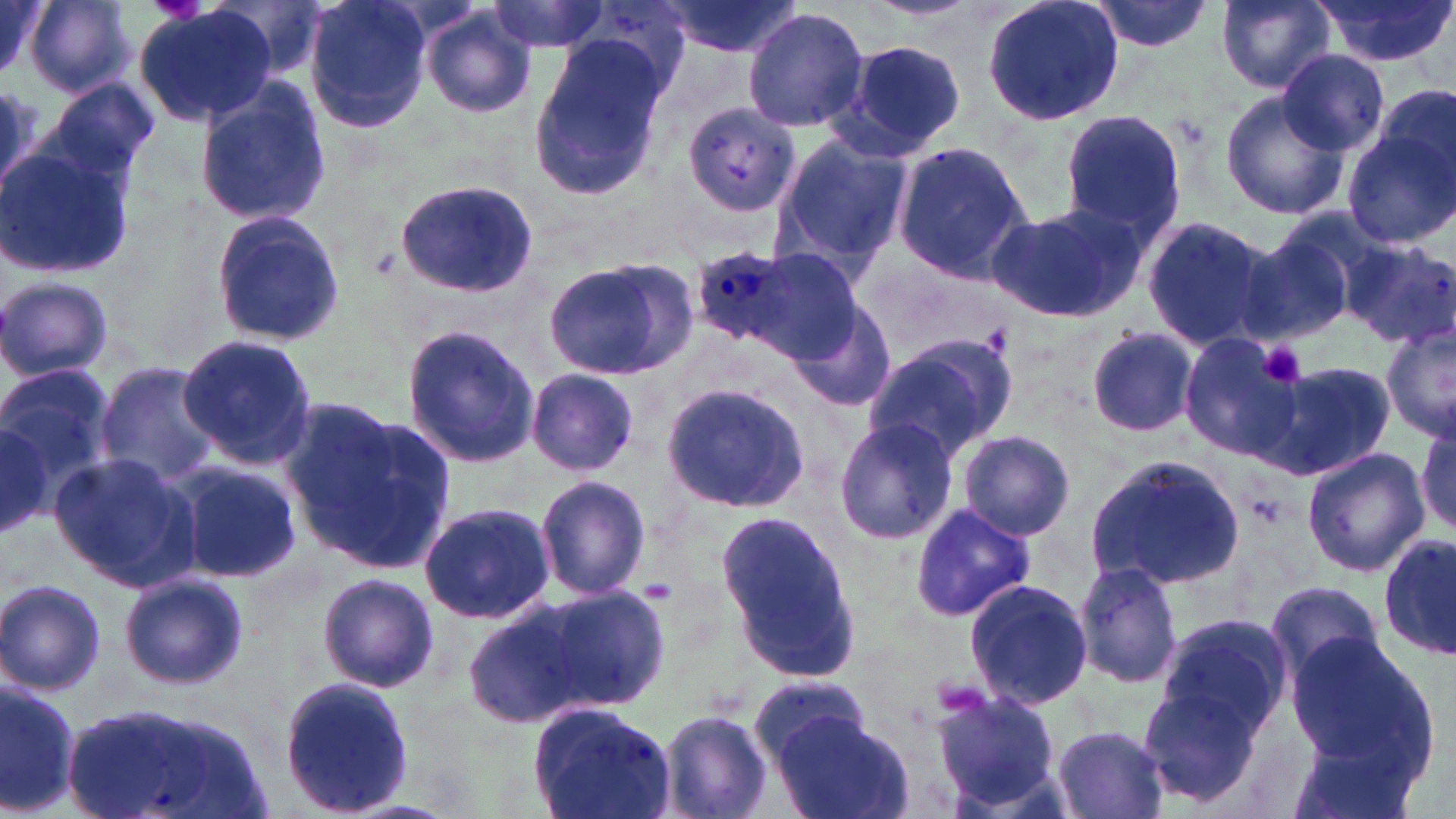 Approximate bounding boxes as [x1, y1, x2, y2] in pixels. Plasmodium ovale-infected red blood cell locations: [693, 245, 795, 345]. Uninfected red blood cell locations: [0, 0, 44, 78], [26, 0, 133, 96], [211, 0, 332, 81], [304, 0, 434, 136], [657, 0, 808, 59], [980, 0, 1124, 126], [1089, 0, 1214, 55], [1214, 0, 1339, 92], [1309, 0, 1455, 68], [484, 1, 615, 55], [135, 6, 276, 128], [420, 8, 537, 119], [743, 8, 870, 135], [527, 36, 671, 200], [835, 39, 966, 163], [1277, 49, 1388, 157], [0, 78, 57, 192], [41, 78, 159, 187], [194, 81, 331, 226], [1367, 82, 1456, 212], [1218, 93, 1349, 220], [679, 103, 804, 221], [1058, 110, 1186, 236], [1340, 124, 1456, 249], [773, 134, 912, 268], [890, 139, 1034, 286], [0, 143, 134, 280], [394, 179, 537, 298], [988, 202, 1145, 323], [210, 210, 344, 346], [1141, 215, 1276, 353], [1232, 231, 1357, 349], [1339, 239, 1455, 347], [766, 251, 857, 367], [544, 256, 699, 382], [0, 276, 115, 380], [790, 303, 899, 412], [399, 323, 543, 472], [1382, 325, 1456, 444], [1083, 326, 1199, 438], [177, 333, 320, 471], [862, 334, 1015, 460], [1178, 335, 1304, 460], [1266, 361, 1395, 481], [0, 362, 116, 503], [93, 362, 222, 487], [527, 368, 639, 476], [660, 381, 810, 514], [291, 407, 457, 574], [0, 414, 56, 541], [833, 419, 959, 543], [1415, 424, 1454, 536], [956, 429, 1076, 541], [1301, 446, 1430, 577], [48, 452, 198, 590], [1084, 453, 1245, 589], [175, 463, 302, 582], [535, 474, 652, 601], [419, 502, 556, 624], [909, 504, 1038, 623], [718, 512, 864, 683], [1380, 535, 1454, 660], [1072, 562, 1183, 691], [118, 572, 249, 691], [317, 572, 439, 693], [0, 579, 107, 694], [962, 579, 1094, 710], [1265, 581, 1388, 685], [534, 583, 672, 714], [464, 604, 593, 730], [1153, 612, 1291, 745], [1284, 632, 1434, 775], [749, 675, 871, 767], [279, 676, 413, 814], [0, 678, 81, 816], [1134, 679, 1270, 808], [932, 685, 1068, 812], [61, 699, 268, 817], [529, 701, 676, 819], [655, 710, 774, 819], [773, 713, 913, 819], [1051, 725, 1173, 819]. Platelet locations: [1258, 342, 1305, 387], [639, 579, 680, 603]. Slide-level diagnosis: Plasmodium ovale. Single field of view. May-Grünwald-Giemsa stain. Captured at 1000x magnification. Light microscopy. Thin blood smear. Image is 1456×819 pixels.